Assess the morphology of the erythrocytes.
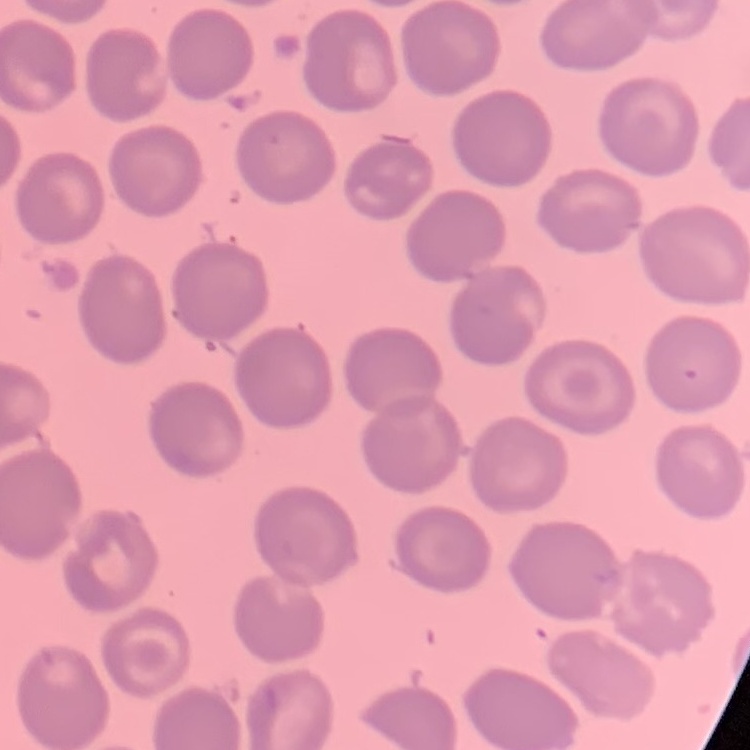

They show no rouleaux formation.

stain: Field's or Giemsa
preparation: thin peripheral smear
image_type: one tile cut from a larger photomicrograph